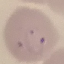

Summary:
  - Malaria status: parasitized
  - Capture: smartphone through the microscope eyepiece
  - Preparation: thin blood film
  - Stain: Giemsa
  - Image type: automatically extracted cell patch, resized to 64 × 64 pixels